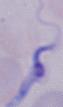

{
  "identification": "trypanosome",
  "modality": "micrograph",
  "magnification": "1000x"
}